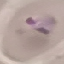
Malaria status: parasitized. Photographed with a smartphone camera at the microscope eyepiece. Giemsa-stained preparation. Automatically extracted cell patch, resized to 64 × 64 pixels. Thin smear of blood.